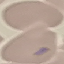

Summary:
  - Malaria status: uninfected
  - Image type: cell patch, automatically extracted from a larger field of view and resized to 64 × 64 pixels
  - Stain: Giemsa
  - Preparation: thin blood film
  - Capture: smartphone through the microscope eyepiece